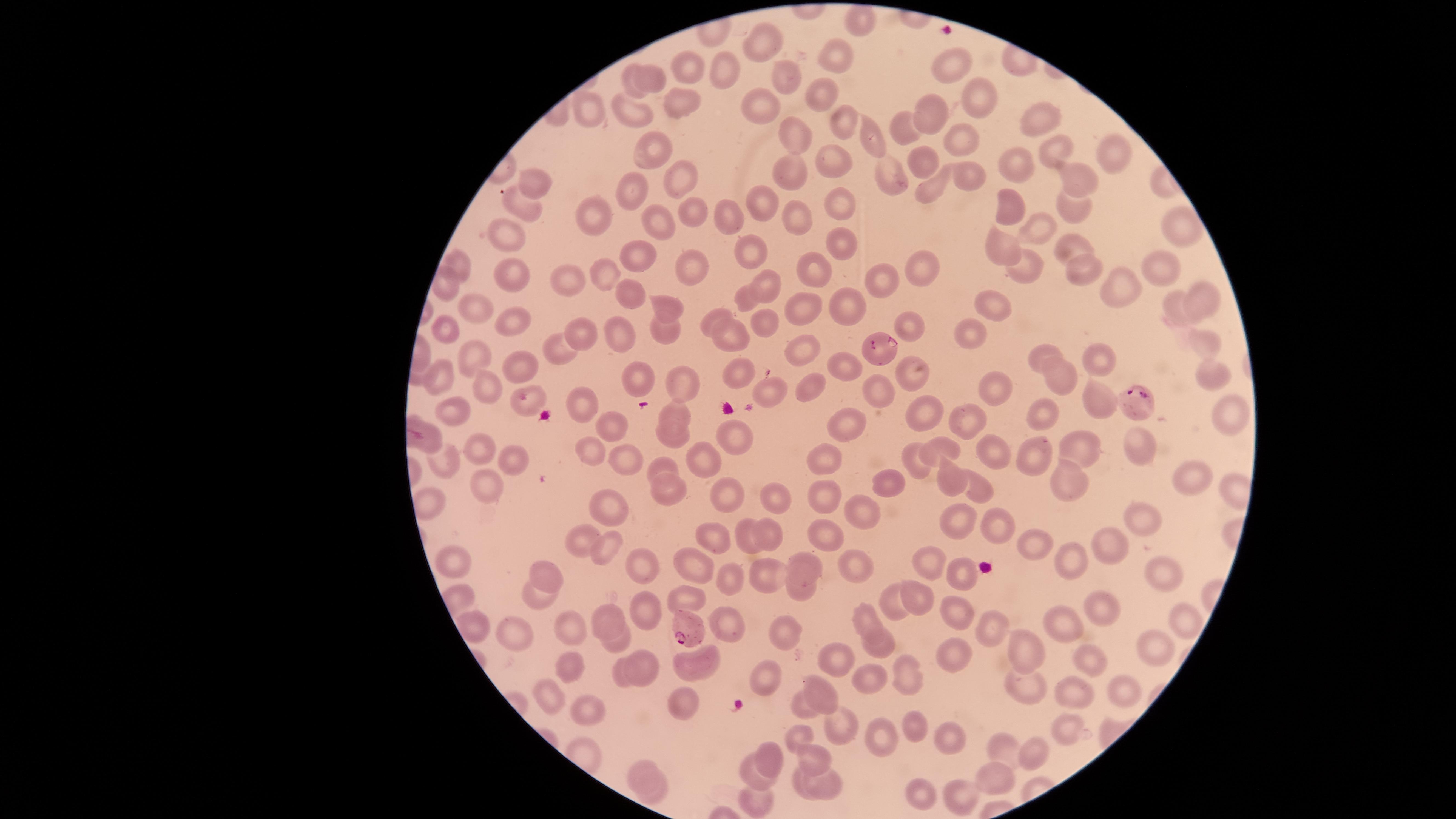

Approximate marker points, in pixels from the top-left corner.
Summary:
  - Parasitized red blood cells: (x=883, y=351), (x=1134, y=397), (x=691, y=628)
  - Uninfected red blood cells: (x=858, y=24), (x=764, y=45), (x=839, y=64), (x=688, y=66), (x=951, y=66), (x=725, y=67), (x=648, y=70), (x=778, y=81), (x=633, y=87), (x=971, y=91), (x=823, y=97), (x=682, y=105), (x=755, y=105), (x=582, y=110), (x=632, y=111), (x=930, y=116), (x=1043, y=116), (x=839, y=125), (x=794, y=131), (x=903, y=132), (x=962, y=136), (x=876, y=137), (x=1049, y=147), (x=1114, y=151), (x=652, y=153), (x=1017, y=158), (x=930, y=165), (x=835, y=166), (x=792, y=170), (x=883, y=171), (x=972, y=173), (x=1084, y=174), (x=674, y=175), (x=540, y=182), (x=931, y=188), (x=630, y=189), (x=769, y=199), (x=1007, y=201), (x=687, y=204), (x=522, y=206), (x=840, y=206), (x=1074, y=207), (x=592, y=209), (x=790, y=212), (x=661, y=216), (x=729, y=216), (x=1175, y=223), (x=1043, y=224), (x=510, y=229), (x=744, y=238), (x=840, y=241), (x=1069, y=243), (x=990, y=248), (x=635, y=253), (x=911, y=259), (x=459, y=262), (x=684, y=262), (x=1078, y=262), (x=1163, y=262), (x=1028, y=267), (x=603, y=269), (x=814, y=270), (x=883, y=278), (x=573, y=279), (x=762, y=279), (x=510, y=280), (x=1117, y=284), (x=443, y=285), (x=628, y=289), (x=748, y=293), (x=1196, y=295), (x=997, y=300), (x=1178, y=303), (x=666, y=304), (x=844, y=304), (x=798, y=305), (x=480, y=307), (x=510, y=314), (x=763, y=314), (x=717, y=317), (x=663, y=324), (x=440, y=327), (x=909, y=330), (x=732, y=332), (x=583, y=333), (x=626, y=333), (x=974, y=333), (x=803, y=345), (x=558, y=347), (x=1201, y=348), (x=1047, y=353), (x=477, y=355), (x=1099, y=359), (x=848, y=360), (x=522, y=361), (x=742, y=366), (x=907, y=370), (x=438, y=375), (x=1061, y=377), (x=642, y=378), (x=1204, y=378), (x=682, y=379), (x=987, y=384), (x=481, y=385), (x=807, y=385), (x=772, y=388), (x=881, y=391), (x=1094, y=398), (x=583, y=405), (x=452, y=408), (x=680, y=409), (x=1227, y=409), (x=928, y=411), (x=1041, y=411), (x=967, y=415), (x=846, y=421), (x=611, y=422), (x=672, y=431), (x=738, y=436), (x=1145, y=443), (x=990, y=447), (x=1087, y=447), (x=485, y=448), (x=591, y=452), (x=936, y=452), (x=1029, y=456), (x=511, y=458), (x=442, y=459), (x=706, y=459), (x=624, y=460), (x=816, y=460), (x=917, y=465), (x=662, y=466), (x=1188, y=476), (x=946, y=479), (x=1062, y=479), (x=484, y=480), (x=890, y=486), (x=978, y=487), (x=721, y=489), (x=676, y=491), (x=828, y=496), (x=784, y=500), (x=425, y=501), (x=608, y=504), (x=860, y=515), (x=1144, y=520), (x=989, y=523), (x=955, y=524), (x=775, y=533), (x=826, y=533), (x=745, y=534), (x=722, y=536), (x=576, y=540), (x=1028, y=543), (x=1107, y=547), (x=602, y=548), (x=453, y=555), (x=931, y=557), (x=636, y=560), (x=1076, y=560), (x=804, y=564), (x=697, y=565), (x=858, y=572), (x=1161, y=572), (x=556, y=573), (x=768, y=575), (x=960, y=578), (x=730, y=581), (x=804, y=587), (x=919, y=594), (x=538, y=598), (x=690, y=600), (x=898, y=600), (x=1098, y=601), (x=961, y=609), (x=638, y=610), (x=613, y=612), (x=867, y=618), (x=1174, y=618), (x=1063, y=620), (x=724, y=622), (x=473, y=625), (x=576, y=627), (x=991, y=627), (x=785, y=628), (x=525, y=629), (x=619, y=643), (x=881, y=643), (x=1155, y=645), (x=1025, y=651), (x=835, y=656), (x=705, y=658), (x=1087, y=659), (x=641, y=664), (x=574, y=667), (x=681, y=670), (x=625, y=671), (x=870, y=675), (x=905, y=676), (x=766, y=678), (x=1012, y=681), (x=1118, y=691), (x=1077, y=692), (x=553, y=694), (x=682, y=696), (x=820, y=697), (x=589, y=702), (x=802, y=703), (x=837, y=723), (x=914, y=728), (x=1069, y=730), (x=801, y=731), (x=945, y=734), (x=879, y=737), (x=1037, y=750), (x=1012, y=751), (x=771, y=753), (x=818, y=755), (x=644, y=769), (x=995, y=777), (x=754, y=778), (x=798, y=778), (x=825, y=779), (x=659, y=790), (x=759, y=793), (x=923, y=795), (x=957, y=801)
  - Preparation: thin smear of blood
  - Stain: Giemsa
  - Field of view: single
  - Capture: smartphone photograph through the microscope eyepiece
  - Image size: 1456×819 pixels
  - Visible region: circular
  - Species: Plasmodium falciparum
  - Presence: malaria parasites seen